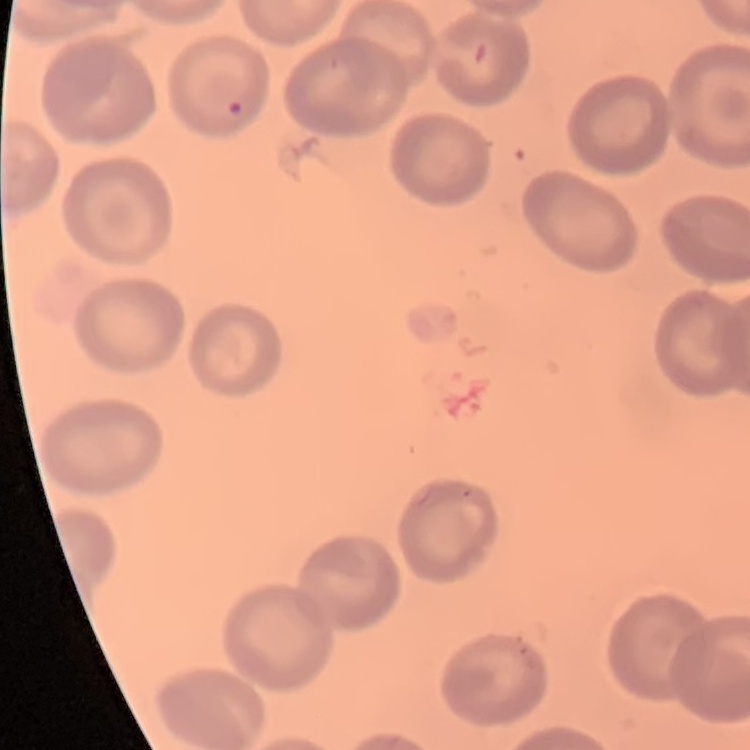

Summary:
  - Red blood cell morphology: no rouleaux formation
  - Image type: one tile cut from a larger photomicrograph
  - Preparation: thin peripheral smear
  - Stain: Field's or Giemsa